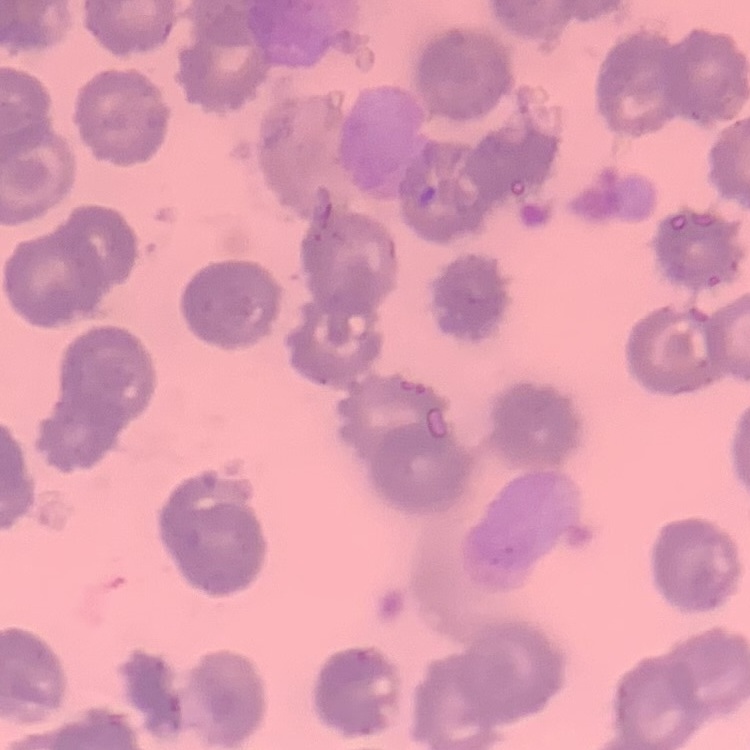

Summary:
  - Red blood cell morphology: no rouleaux formation
  - Preparation: thin blood film
  - Image type: one tile cut from a larger photomicrograph
  - Stain: Field's or Giemsa